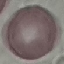

malaria status = uninfected
stain = Giemsa
image type = automatically extracted cell patch, resized to 64 × 64 pixels
preparation = thin blood smear
capture = smartphone through the microscope eyepiece